Locate and identify every blood parasite.
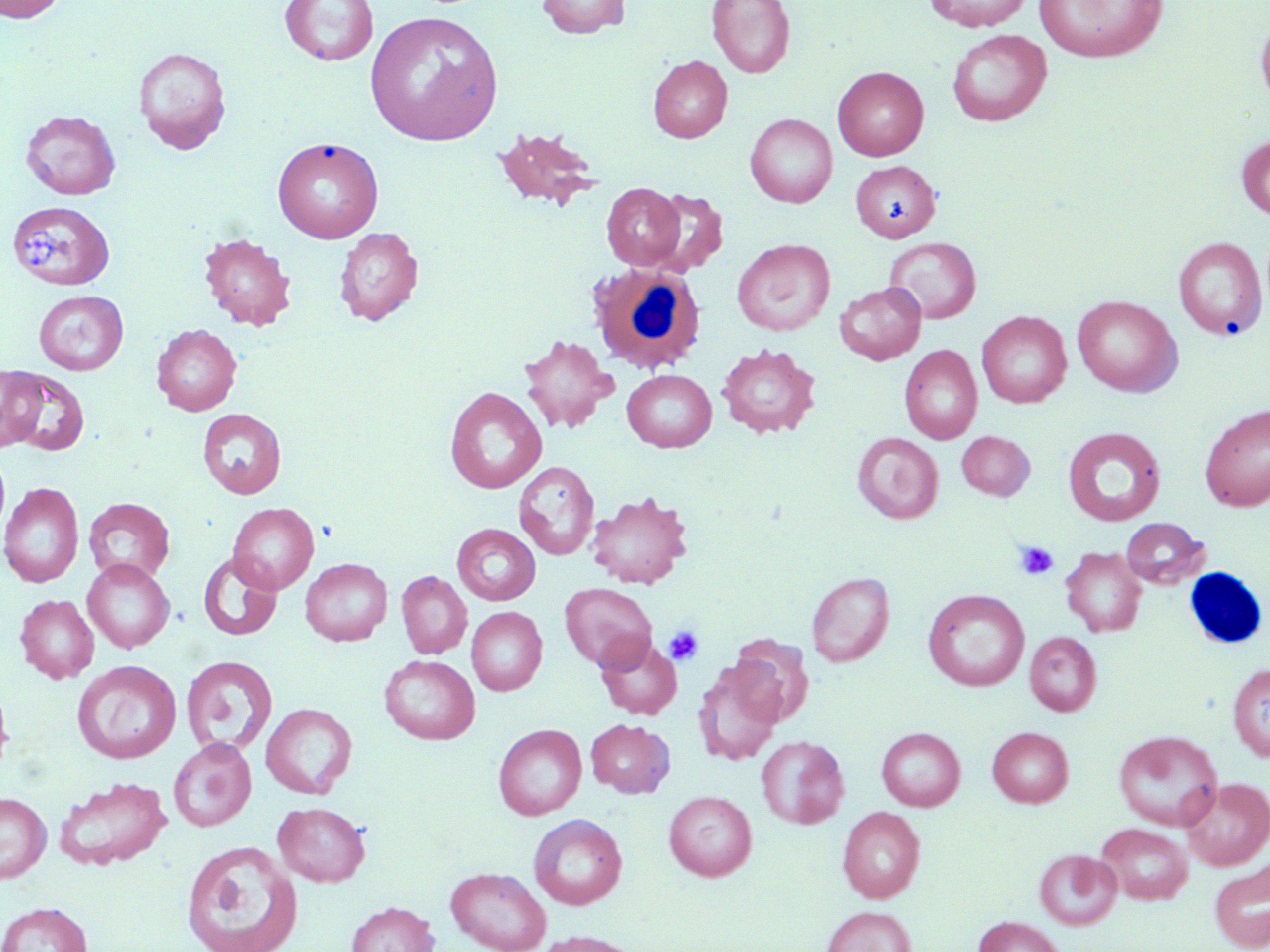
No blood parasites seen.

Summary:
  - Coordinate format: approximate bounding boxes as (x1, y1, x2, y2) in pixels
  - Platelet locations: (21, 225, 62, 268), (1014, 541, 1058, 581), (663, 625, 704, 666)
  - Uninfected red blood cell locations: (0, 0, 66, 24), (280, 0, 379, 66), (536, 0, 630, 38), (707, 0, 795, 78), (923, 0, 1033, 31), (1034, 0, 1167, 63), (1255, 8, 1270, 112), (365, 10, 504, 146), (947, 29, 1052, 126), (133, 46, 231, 154), (647, 55, 733, 143), (833, 66, 929, 161), (21, 109, 120, 200), (745, 113, 837, 208), (492, 125, 602, 212), (1236, 135, 1270, 221), (273, 136, 383, 243), (850, 160, 940, 242), (601, 183, 685, 269), (645, 188, 728, 275), (9, 201, 116, 287), (334, 227, 423, 325), (198, 232, 297, 330), (1173, 236, 1267, 340), (884, 237, 982, 323), (732, 238, 835, 336), (835, 281, 926, 365), (33, 290, 128, 375), (1072, 295, 1182, 397), (977, 311, 1072, 407), (151, 323, 241, 416), (518, 334, 618, 435), (715, 343, 820, 439), (899, 344, 982, 444), (619, 363, 814, 447), (0, 366, 46, 451), (4, 368, 90, 456), (622, 369, 717, 452), (445, 386, 547, 494), (1199, 403, 1270, 511), (197, 408, 287, 499), (1062, 427, 1166, 526), (957, 431, 1035, 501), (852, 432, 944, 524), (514, 461, 599, 561), (0, 482, 84, 588), (587, 491, 693, 589), (83, 497, 175, 585), (228, 502, 319, 594), (1120, 518, 1210, 588), (452, 524, 541, 606), (1060, 547, 1147, 636), (198, 552, 283, 641), (300, 557, 392, 646), (82, 558, 174, 653), (397, 570, 472, 658), (806, 571, 894, 667), (559, 582, 657, 671), (923, 589, 1029, 691), (15, 594, 99, 684), (466, 607, 548, 695), (1025, 632, 1102, 716), (595, 635, 682, 719), (729, 635, 814, 726), (180, 655, 278, 756), (380, 655, 480, 744), (72, 660, 181, 764), (693, 661, 784, 766), (1227, 664, 1270, 762), (0, 679, 13, 781), (260, 703, 357, 799), (586, 718, 674, 798), (492, 723, 587, 820), (987, 726, 1074, 807), (877, 727, 965, 811), (1113, 730, 1223, 831), (756, 735, 849, 829), (168, 736, 257, 831), (55, 776, 172, 870), (1182, 777, 1270, 870), (664, 790, 757, 881), (0, 792, 51, 883), (273, 802, 370, 886), (837, 807, 925, 903), (528, 813, 627, 910), (1096, 823, 1193, 905), (181, 839, 302, 952), (1035, 848, 1121, 929), (1210, 861, 1270, 952), (445, 866, 551, 952), (345, 901, 439, 952), (0, 902, 93, 952), (822, 906, 917, 952), (973, 916, 1066, 952), (531, 930, 646, 952)
  - White blood cell locations: (587, 259, 704, 376)
  - Slide-level diagnosis: no evidence of blood parasites
  - Image size: 1270×952 pixels
  - Preparation: thin blood smear
  - Stain: May-Grünwald-Giemsa
  - Field of view: one of a larger specimen
  - Modality: optical microscopy
  - Magnification: 1000x